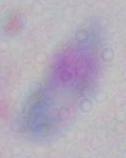
identification = Toxoplasma gondii
modality = photomicrograph
magnification = 1000x